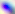

Summary:
  - Magnification: 400x
  - Identification: Toxoplasma gondii
  - Modality: micrograph